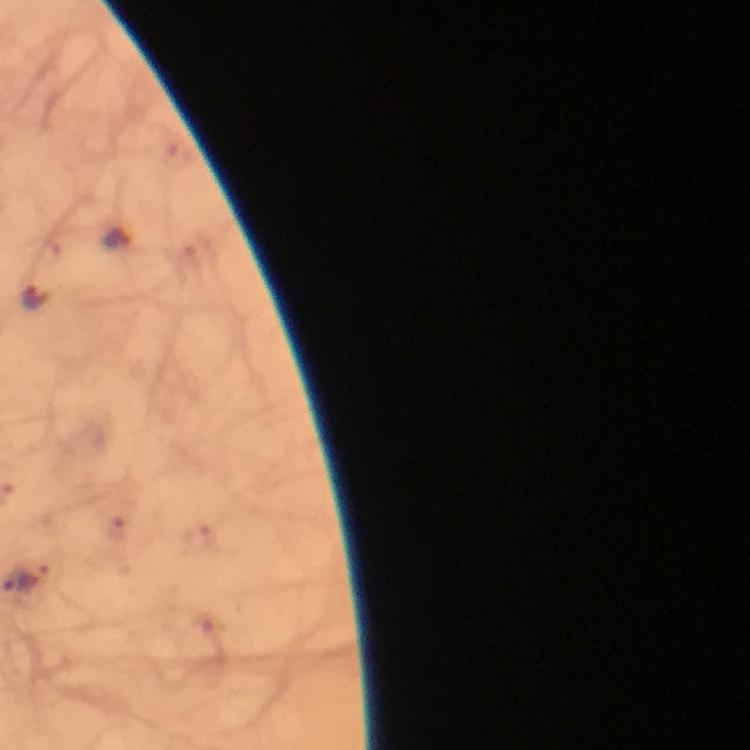 Approximate centers as (x, y) in pixels. Malaria parasite locations: (120, 238), (35, 299). Image is 750×750 pixels. 100x magnification. From a malaria diagnostic workup. Immersion oil applied. Thick blood smear. Giemsa stain. A crop from one field of view. Photographed with a smartphone mounted on the microscope.